Locate every blood parasite and identify its species.
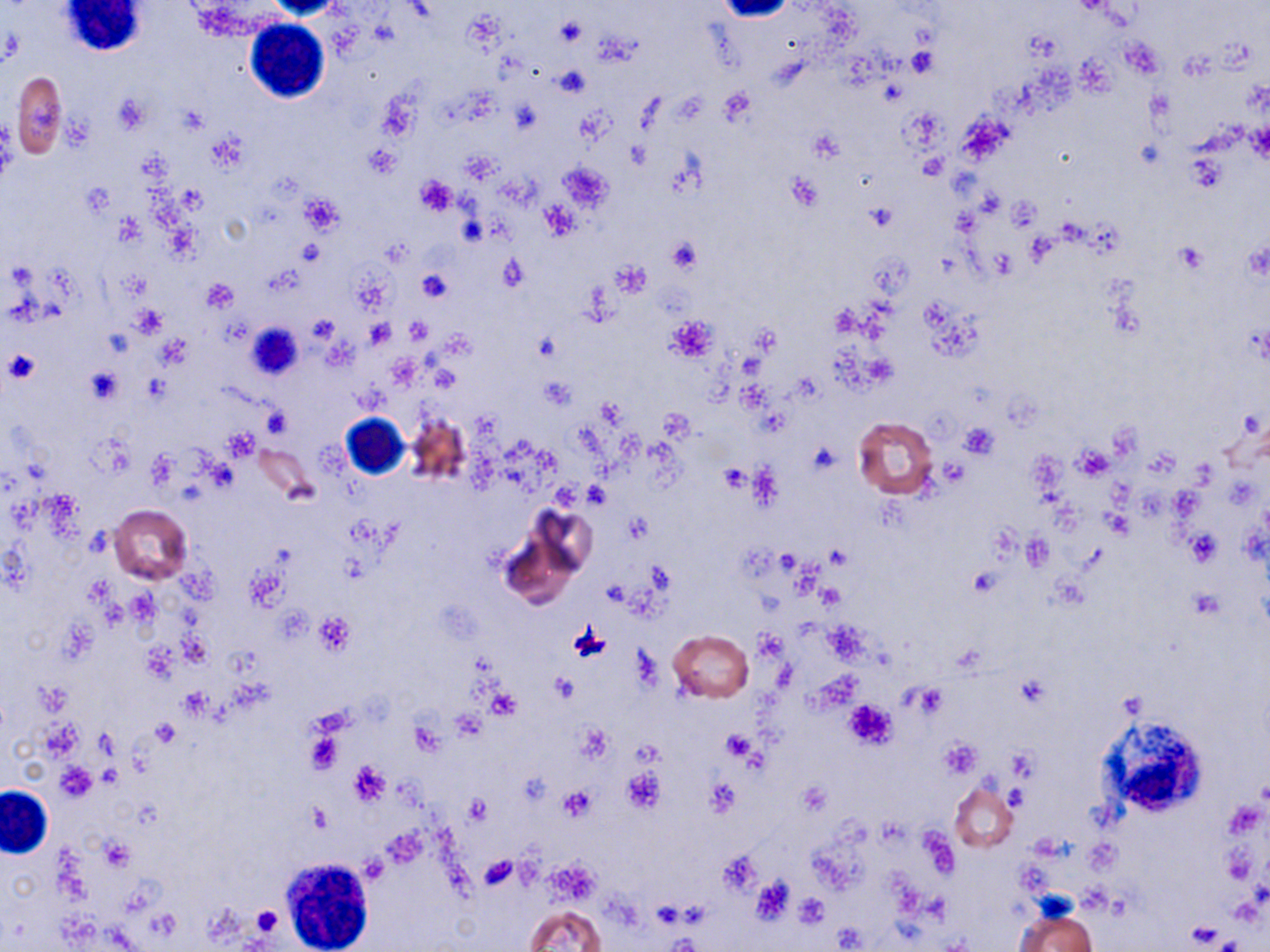

No blood parasites seen.

Summary:
  - Coordinate format: approximate bounding boxes as (x1, y1, x2, y2) in pixels
  - White blood cell locations: (59, 0, 146, 59), (246, 19, 330, 103), (341, 411, 412, 481), (1100, 717, 1208, 817), (0, 785, 53, 857), (280, 857, 375, 948)
  - Uninfected red blood cell locations: (10, 71, 68, 159), (406, 412, 472, 489), (851, 416, 938, 499), (252, 444, 315, 499), (109, 503, 193, 585), (529, 505, 599, 588), (668, 630, 753, 703), (950, 782, 1018, 852), (525, 905, 605, 952), (1015, 908, 1097, 952)
  - Platelet locations: (556, 18, 586, 46), (554, 66, 591, 97), (719, 88, 755, 123), (114, 95, 149, 133), (60, 117, 93, 150), (365, 145, 400, 178), (918, 152, 946, 180), (786, 174, 821, 211), (415, 176, 457, 215), (80, 182, 114, 217), (300, 195, 344, 234), (542, 201, 578, 238), (864, 203, 896, 231), (668, 238, 702, 274), (299, 240, 324, 266), (1174, 242, 1208, 273), (500, 255, 528, 291), (611, 261, 651, 295), (418, 269, 451, 303), (200, 280, 238, 311), (135, 306, 165, 337), (668, 316, 716, 362), (406, 317, 431, 344), (366, 319, 395, 348), (533, 331, 561, 360), (2, 350, 40, 386), (85, 367, 121, 404), (538, 377, 577, 410), (658, 408, 694, 441), (961, 423, 998, 459), (1074, 447, 1113, 479), (719, 463, 749, 494), (585, 482, 611, 508), (1105, 511, 1132, 538), (626, 512, 652, 545), (1185, 530, 1223, 567), (314, 612, 354, 653), (568, 623, 613, 663), (548, 671, 581, 703), (38, 684, 70, 716), (911, 685, 948, 717), (179, 688, 211, 719), (486, 689, 521, 717), (844, 700, 896, 748), (37, 719, 84, 760), (152, 719, 181, 749), (572, 721, 613, 764), (721, 731, 755, 762), (304, 733, 343, 774), (938, 739, 980, 779), (348, 760, 392, 805), (56, 763, 98, 800), (622, 768, 665, 812), (798, 781, 831, 816), (558, 786, 595, 821), (465, 794, 493, 825), (100, 837, 134, 870), (478, 855, 517, 890), (751, 875, 795, 924), (795, 893, 830, 926), (251, 905, 281, 937), (1186, 921, 1224, 947), (669, 936, 702, 952)
  - Slide-level diagnosis: no evidence of blood parasites
  - Modality: light microscopy
  - Field of view: single
  - Image size: 1270×952 pixels
  - Magnification: 1000x
  - Stain: May-Grünwald-Giemsa
  - Preparation: thin blood smear